Assess the morphology of the red blood cells.
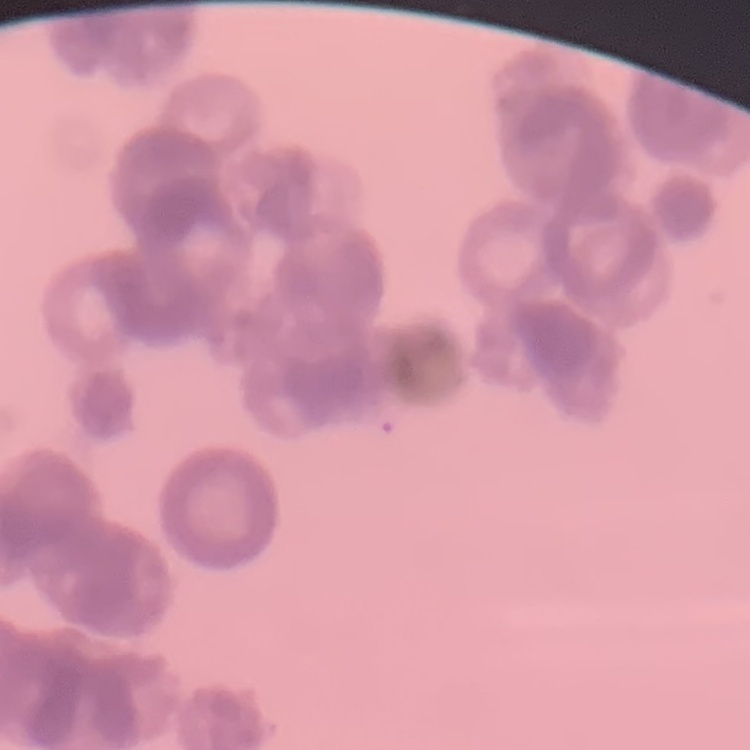
They show rouleaux formation.

stain = Field's or Giemsa
image type = one tile cut from a larger photomicrograph
preparation = thin peripheral smear